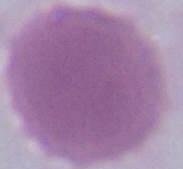
An erythrocyte is seen. 1000x magnification. Photomicrograph.